Report the malaria status of this cell.
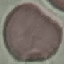

It is uninfected.

Thin blood film. Giemsa-stained preparation. Cell patch, automatically extracted from a larger field of view and resized to 64 × 64 pixels. Acquired by smartphone through the microscope eyepiece.